Point out each leukocyte.
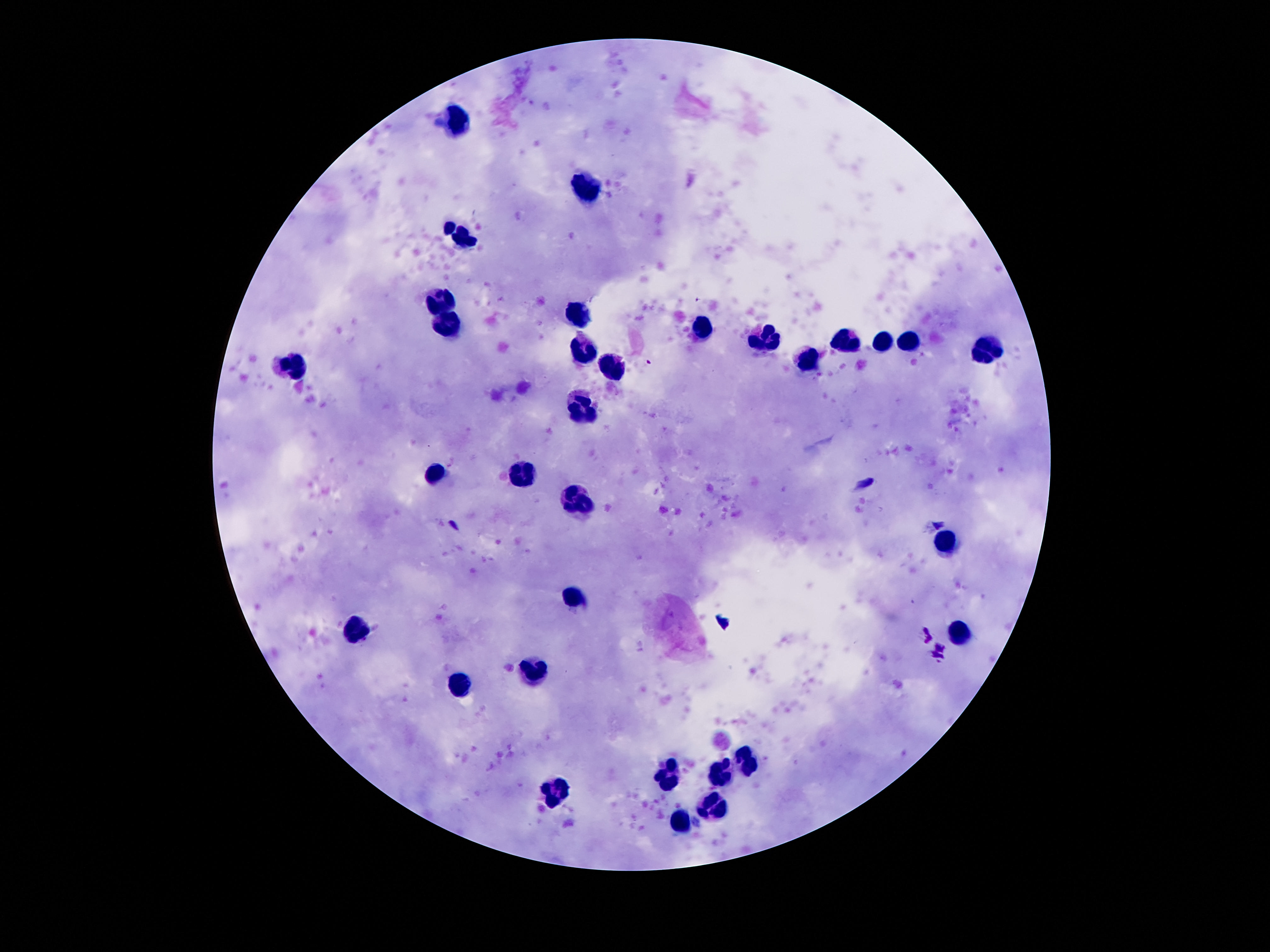
Approximate object centers, in pixels from the top-left corner.
Leukocytes: (x=461, y=123), (x=589, y=187), (x=459, y=238), (x=441, y=300), (x=578, y=314), (x=447, y=322), (x=701, y=326), (x=845, y=339), (x=769, y=342), (x=881, y=342), (x=910, y=344), (x=588, y=350), (x=988, y=350), (x=808, y=359), (x=296, y=365), (x=609, y=368), (x=582, y=409), (x=433, y=474), (x=521, y=475), (x=580, y=502), (x=947, y=543), (x=574, y=597), (x=357, y=628), (x=959, y=630), (x=531, y=674), (x=461, y=684), (x=746, y=762), (x=668, y=774), (x=718, y=777), (x=552, y=792), (x=709, y=807), (x=679, y=823).

stain: Giemsa
field_of_view: one from this slide
magnification: 100x
patient_malaria_status: uninfected
image_size: 1270×952 pixels
capture: smartphone camera through the microscope eyepiece
preparation: thick blood film